Identify the cell.
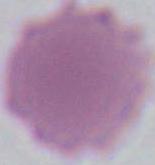

This is an erythrocyte.

Summary:
  - Modality: micrograph
  - Magnification: 1000x